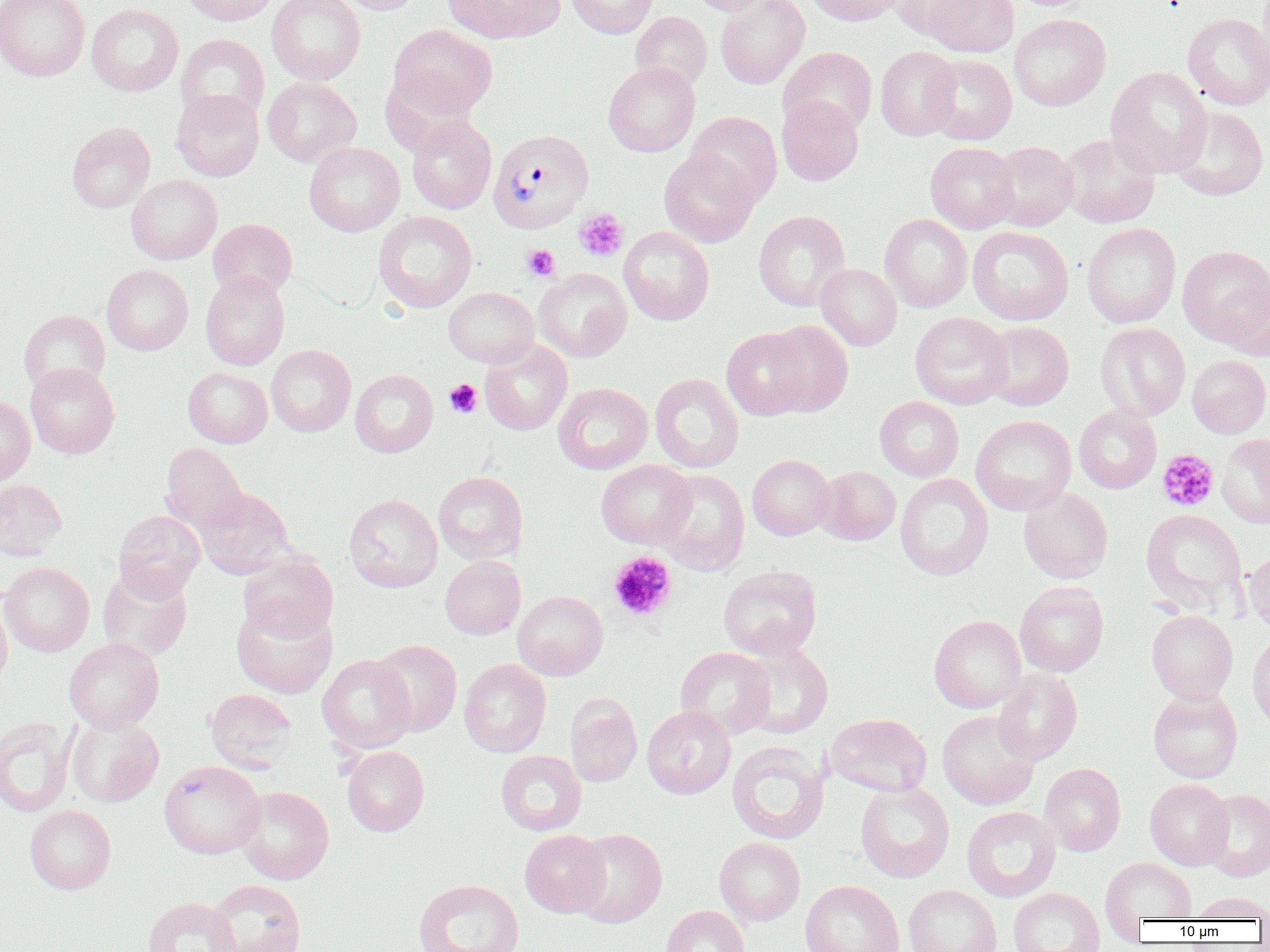 Approximate bounding boxes as [x1, y1, x2, y2] in pixels. Plasmodium vivax-infected red blood cell locations: [488, 128, 594, 233]. Uninfected red blood cell locations: [0, 0, 90, 81], [182, 0, 279, 26], [267, 0, 364, 84], [335, 0, 425, 15], [443, 0, 565, 43], [566, 0, 659, 38], [689, 0, 775, 16], [715, 0, 809, 89], [804, 0, 907, 26], [922, 0, 1019, 57], [894, 1, 988, 42], [86, 3, 184, 96], [630, 11, 712, 92], [1009, 14, 1111, 111], [1183, 14, 1270, 110], [388, 25, 497, 119], [176, 34, 269, 124], [778, 46, 877, 137], [876, 46, 961, 141], [924, 54, 1017, 145], [603, 62, 700, 157], [1106, 66, 1212, 177], [379, 73, 481, 155], [262, 77, 361, 166], [171, 89, 264, 181], [777, 96, 863, 186], [1168, 106, 1269, 201], [686, 111, 782, 206], [407, 115, 496, 214], [67, 122, 156, 212], [1058, 133, 1160, 228], [989, 141, 1078, 231], [304, 142, 404, 236], [925, 142, 1019, 234], [659, 150, 759, 247], [126, 175, 222, 264], [373, 210, 477, 312], [753, 210, 851, 311], [879, 214, 973, 312], [208, 219, 298, 300], [1081, 223, 1181, 328], [619, 226, 714, 325], [967, 226, 1074, 325], [1177, 245, 1269, 348], [102, 264, 193, 355], [815, 264, 902, 350], [534, 268, 632, 362], [200, 271, 290, 370], [1223, 273, 1270, 361], [443, 287, 539, 368], [18, 310, 110, 396], [909, 312, 1013, 410], [762, 320, 853, 417], [980, 321, 1074, 410], [1095, 323, 1191, 421], [721, 326, 813, 420], [480, 340, 572, 436], [266, 344, 356, 437], [1187, 355, 1270, 438], [25, 363, 120, 459], [183, 367, 273, 448], [350, 369, 438, 457], [650, 372, 744, 473], [553, 382, 653, 474], [0, 395, 35, 485], [875, 396, 964, 481], [1074, 405, 1162, 494], [971, 415, 1076, 515], [1217, 433, 1270, 528], [160, 443, 248, 532], [747, 454, 835, 540], [596, 459, 696, 548], [816, 466, 901, 545], [654, 469, 750, 574], [433, 471, 528, 564], [895, 473, 994, 581], [0, 478, 68, 560], [195, 488, 294, 576], [1019, 488, 1113, 583], [344, 494, 442, 592], [1141, 509, 1246, 609], [113, 510, 205, 600], [1243, 548, 1270, 633], [238, 554, 338, 643], [439, 556, 526, 639], [0, 562, 94, 656], [718, 565, 822, 659], [97, 568, 193, 660], [1014, 581, 1109, 677], [513, 590, 608, 680], [0, 593, 12, 692], [231, 601, 337, 698], [1146, 610, 1238, 703], [928, 615, 1026, 713], [1247, 631, 1270, 729], [63, 638, 164, 733], [371, 639, 462, 736], [736, 644, 833, 739], [675, 647, 775, 740], [317, 654, 416, 754], [459, 659, 551, 757], [993, 669, 1083, 765], [205, 688, 297, 772], [1147, 688, 1243, 783], [565, 694, 643, 786], [642, 706, 735, 799], [937, 710, 1039, 810], [826, 713, 932, 797], [66, 715, 164, 807], [0, 718, 74, 817], [727, 741, 830, 845], [342, 746, 429, 836], [495, 750, 586, 835], [159, 760, 265, 859], [1039, 763, 1126, 856], [1145, 778, 1233, 869], [855, 782, 954, 883], [235, 786, 334, 885], [1199, 788, 1270, 882], [25, 805, 116, 894], [962, 806, 1061, 902], [569, 828, 667, 928], [520, 830, 609, 917], [714, 836, 805, 926], [1100, 857, 1197, 925], [414, 878, 524, 951], [205, 880, 306, 952], [800, 880, 904, 952], [903, 884, 1002, 952], [1008, 887, 1105, 952], [1190, 891, 1270, 921], [143, 897, 242, 952], [660, 905, 750, 952]. Platelet locations: [574, 208, 629, 262], [522, 244, 560, 281], [444, 379, 482, 418], [1157, 449, 1219, 511], [608, 551, 676, 621]. Slide-level diagnosis: Plasmodium vivax. Thin blood film. Image is 1270×952 pixels. Light microscopy. 1000x magnification. One field of a larger specimen.